State which cell type is depicted.
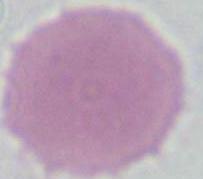
An erythrocyte.

1000x magnification. Photomicrograph.